Give the location of every parasitized red blood cell.
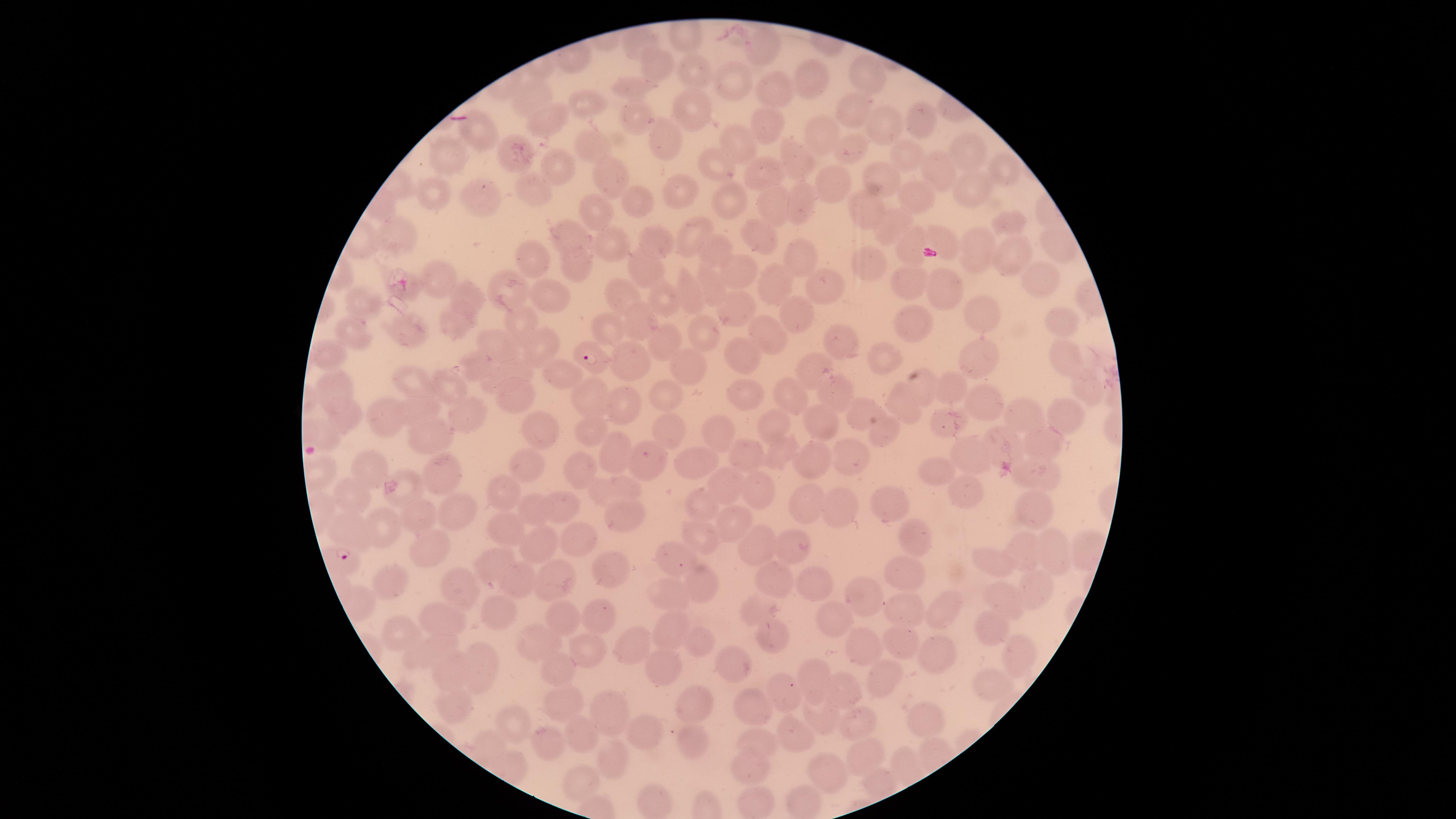

Approximate marker points as [x, y] in pixels.
Parasitized red blood cells: [592, 356], [345, 558].

Approximate marker points as [x, y] in pixels.
Summary:
  - Uninfected red blood cells: [637, 41], [760, 44], [651, 63], [696, 68], [869, 75], [807, 78], [736, 83], [632, 87], [780, 93], [537, 96], [584, 103], [696, 109], [854, 110], [641, 118], [919, 120], [551, 121], [769, 125], [890, 125], [825, 130], [478, 134], [670, 138], [740, 142], [592, 144], [849, 148], [967, 150], [905, 153], [510, 155], [797, 156], [449, 158], [558, 163], [718, 165], [1001, 167], [941, 174], [765, 175], [615, 176], [880, 180], [531, 185], [832, 185], [684, 187], [975, 191], [432, 193], [916, 195], [479, 196], [724, 196], [771, 199], [796, 201], [635, 202], [870, 209], [601, 211], [1011, 219], [894, 225], [403, 232], [691, 232], [759, 233], [570, 234], [941, 237], [614, 239], [656, 240], [912, 243], [1057, 245], [975, 248], [531, 254], [716, 254], [1014, 255], [797, 256], [868, 260], [577, 261], [640, 264], [736, 273], [1044, 276], [441, 279], [904, 282], [710, 284], [826, 285], [409, 286], [950, 286], [510, 288], [770, 288], [623, 293], [553, 295], [688, 295], [466, 297], [665, 299], [362, 305], [735, 308], [978, 312], [799, 315], [523, 317], [1061, 318], [909, 322], [639, 323], [452, 324], [607, 326], [345, 332], [409, 332], [704, 332], [770, 334], [837, 338], [665, 340], [498, 342], [539, 342], [330, 352], [1061, 353], [741, 354], [634, 358], [975, 359], [883, 360], [478, 362], [694, 365], [557, 370], [811, 371], [505, 375], [412, 379], [929, 381], [335, 382], [948, 384], [448, 387], [840, 388], [662, 393], [592, 394], [742, 394], [792, 395], [514, 400], [622, 404], [417, 405], [983, 405], [908, 406], [1059, 411], [863, 412], [345, 414], [385, 414], [466, 415], [816, 416], [1026, 416], [944, 421], [774, 424], [883, 427], [592, 428], [667, 428], [536, 429], [720, 430], [320, 434], [427, 438], [1008, 440], [1045, 443], [611, 449], [777, 450], [843, 453], [746, 454], [816, 457], [976, 457], [699, 461], [369, 462], [581, 469], [1043, 470], [445, 472], [535, 472], [944, 476], [725, 482], [614, 486], [754, 489], [409, 492], [506, 494], [970, 494], [354, 497], [890, 501], [1029, 502], [702, 503], [807, 504], [563, 505], [841, 505], [538, 511], [457, 514], [624, 516], [419, 517], [504, 520], [733, 520], [385, 526], [351, 527], [580, 536], [701, 537], [919, 538], [759, 540], [541, 544], [792, 545], [1049, 546], [1084, 547], [433, 548], [1027, 552], [677, 553], [997, 558], [493, 565], [608, 567], [907, 568], [557, 576], [514, 579], [815, 580], [389, 581], [699, 582], [778, 582], [460, 586], [1031, 586], [668, 592], [861, 594], [1001, 596], [944, 608], [912, 611], [760, 613], [506, 614], [560, 615], [442, 620], [604, 620], [838, 620], [666, 627], [991, 627], [401, 630], [770, 636], [905, 637], [541, 638], [694, 642], [634, 644], [866, 647], [426, 648], [585, 651], [944, 651], [1023, 659], [736, 666], [483, 667], [453, 668], [561, 670], [662, 670], [813, 675], [879, 681], [994, 684], [785, 695], [844, 695], [698, 700], [567, 704], [756, 709], [454, 711], [608, 711], [815, 717], [513, 719], [921, 721], [853, 725], [792, 734], [643, 735], [582, 736], [693, 742], [487, 745], [759, 745], [538, 747], [613, 757], [864, 758], [903, 765], [752, 767], [830, 772], [584, 780], [802, 800], [655, 803], [754, 806]
  - Stain: Giemsa
  - Capture: smartphone photograph through the microscope eyepiece
  - Species: Plasmodium falciparum
  - Image size: 1456×819 pixels
  - Visible region: circular
  - Preparation: thin smear of blood
  - Field of view: single